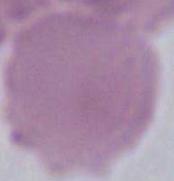

1000x magnification. An erythrocyte is shown. Photomicrograph.